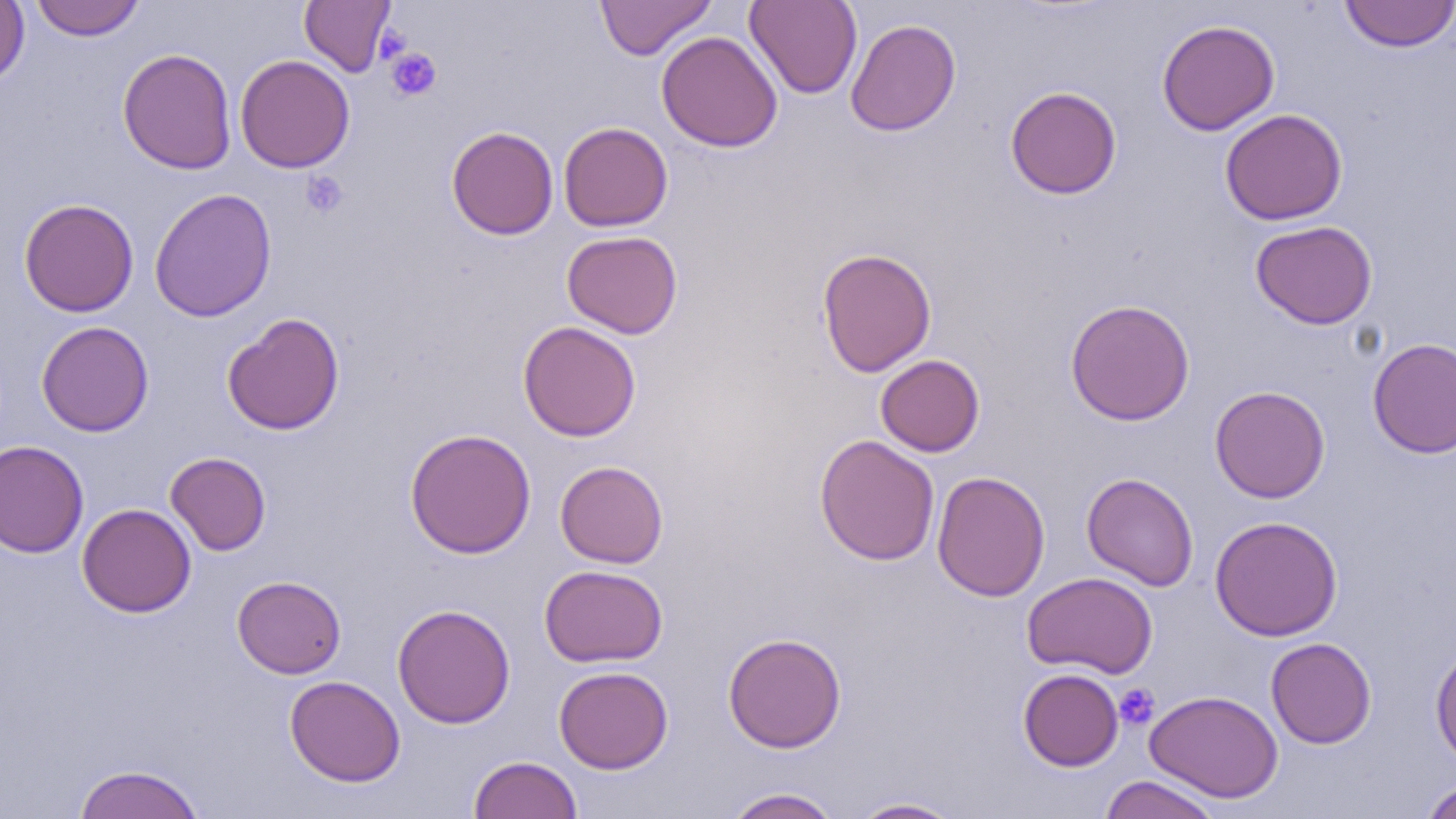

Approximate bounding boxes as named x1/y1/x2/y2 corners in pixels. Platelet locations: (x1=376, y1=26, x2=411, y2=64), (x1=386, y1=47, x2=441, y2=101), (x1=301, y1=171, x2=348, y2=218), (x1=1114, y1=683, x2=1159, y2=730). Uninfected red blood cell locations: (x1=0, y1=0, x2=30, y2=87), (x1=31, y1=0, x2=144, y2=41), (x1=299, y1=0, x2=395, y2=76), (x1=595, y1=0, x2=716, y2=60), (x1=744, y1=0, x2=863, y2=99), (x1=1340, y1=1, x2=1455, y2=52), (x1=846, y1=18, x2=961, y2=136), (x1=1157, y1=19, x2=1280, y2=135), (x1=656, y1=31, x2=783, y2=152), (x1=117, y1=48, x2=237, y2=174), (x1=235, y1=54, x2=355, y2=173), (x1=1005, y1=86, x2=1122, y2=199), (x1=1220, y1=108, x2=1348, y2=226), (x1=558, y1=122, x2=673, y2=232), (x1=446, y1=126, x2=559, y2=240), (x1=149, y1=188, x2=277, y2=322), (x1=19, y1=198, x2=139, y2=316), (x1=1250, y1=220, x2=1378, y2=329), (x1=561, y1=230, x2=682, y2=339), (x1=816, y1=247, x2=937, y2=377), (x1=1065, y1=298, x2=1195, y2=426), (x1=222, y1=313, x2=345, y2=435), (x1=36, y1=320, x2=154, y2=437), (x1=518, y1=321, x2=641, y2=442), (x1=1367, y1=337, x2=1456, y2=458), (x1=875, y1=354, x2=985, y2=457), (x1=1210, y1=386, x2=1331, y2=503), (x1=405, y1=428, x2=537, y2=559), (x1=814, y1=435, x2=940, y2=566), (x1=0, y1=440, x2=89, y2=558), (x1=165, y1=452, x2=271, y2=555), (x1=555, y1=460, x2=669, y2=568), (x1=932, y1=470, x2=1050, y2=602), (x1=1082, y1=472, x2=1199, y2=591), (x1=77, y1=503, x2=196, y2=617), (x1=1210, y1=515, x2=1343, y2=641), (x1=539, y1=564, x2=668, y2=667), (x1=1022, y1=571, x2=1158, y2=678), (x1=232, y1=575, x2=346, y2=678), (x1=392, y1=603, x2=516, y2=728), (x1=723, y1=632, x2=847, y2=753), (x1=1265, y1=637, x2=1377, y2=749), (x1=1430, y1=643, x2=1456, y2=769), (x1=554, y1=665, x2=673, y2=773), (x1=1018, y1=668, x2=1123, y2=771), (x1=284, y1=675, x2=406, y2=787), (x1=1145, y1=690, x2=1284, y2=803), (x1=469, y1=755, x2=582, y2=819), (x1=72, y1=763, x2=206, y2=819), (x1=1098, y1=775, x2=1222, y2=819), (x1=1420, y1=778, x2=1456, y2=819), (x1=723, y1=787, x2=843, y2=818), (x1=849, y1=796, x2=965, y2=818). Slide-level diagnosis: negative for blood parasites. One field of a larger specimen. Thin blood smear. Light microscopy. 1000x magnification. Image is 1456×819 pixels.